Comment on the morphology of the red blood cells.
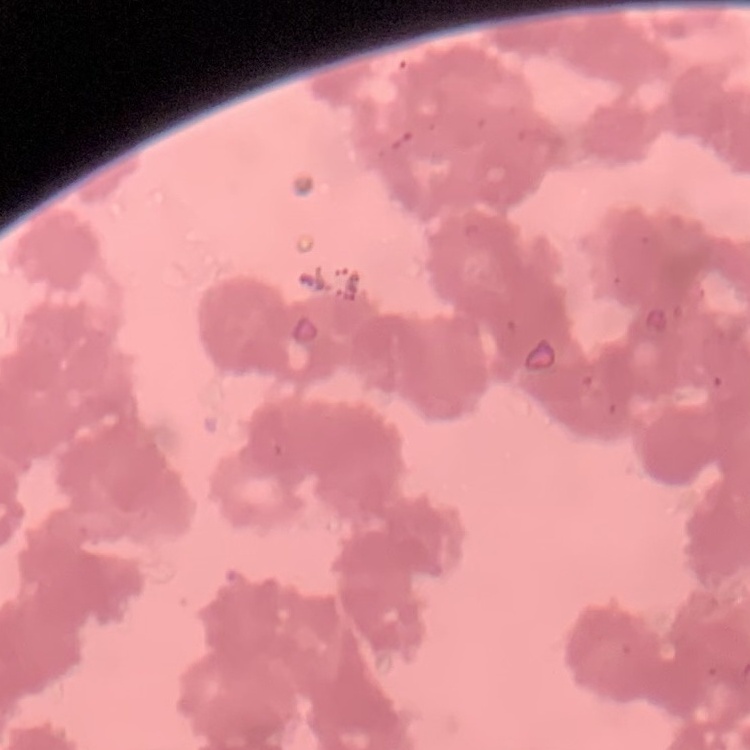

They show rouleaux formation.

Square crop of a larger photomicrograph. Thin peripheral smear. Stained with either Field's or Giemsa.